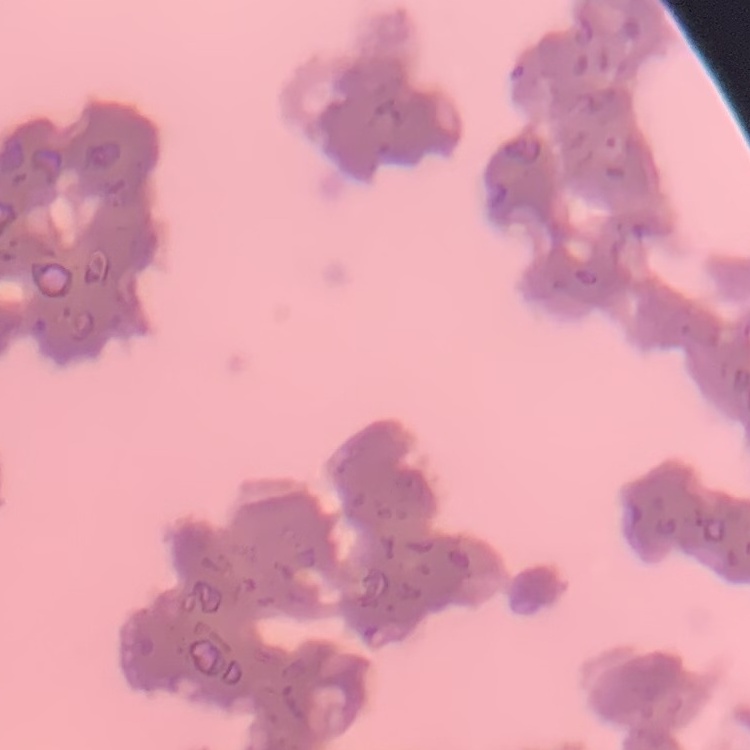
Summary:
  - Red blood cell morphology: rouleaux formation
  - Preparation: thin blood film
  - Image type: square crop of a larger photomicrograph
  - Stain: Field's or Giemsa